Report the malaria status of this cell.
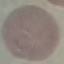

It is uninfected.

Summary:
  - Image type: automatically extracted cell patch, resized to 64 × 64 pixels
  - Preparation: thin blood smear
  - Stain: Giemsa
  - Capture: smartphone through the microscope eyepiece